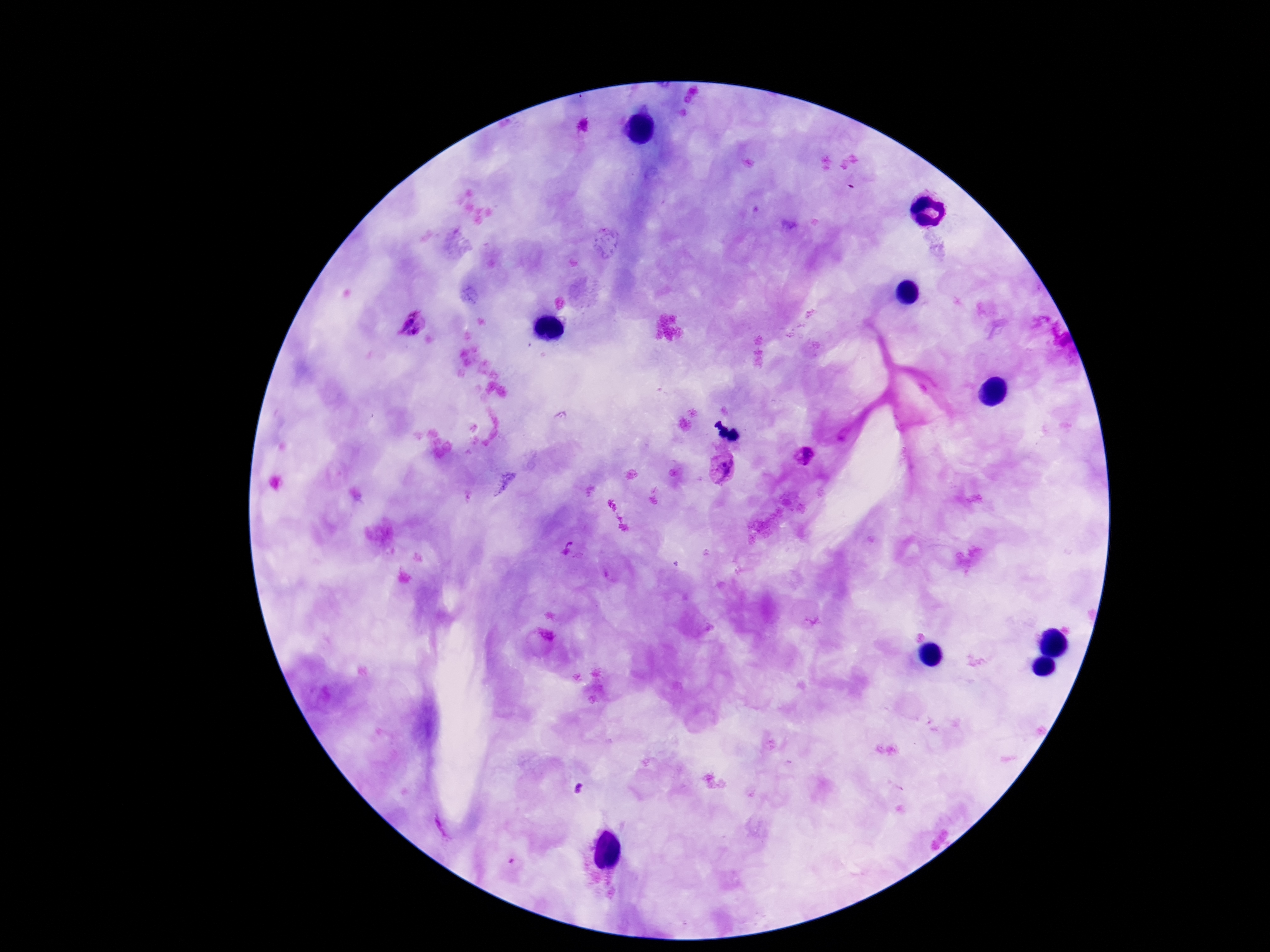
Approximate centers as (x, y) in pixels.
Summary:
  - Plasmodium parasite locations: (582, 128), (414, 325), (806, 457), (723, 467), (569, 547)
  - Capture: smartphone camera through the microscope eyepiece
  - Preparation: thick blood film
  - Field of view: one from this slide
  - Image size: 1270×952 pixels
  - Magnification: 100x
  - Patient malaria status: infected
  - Stain: Giemsa